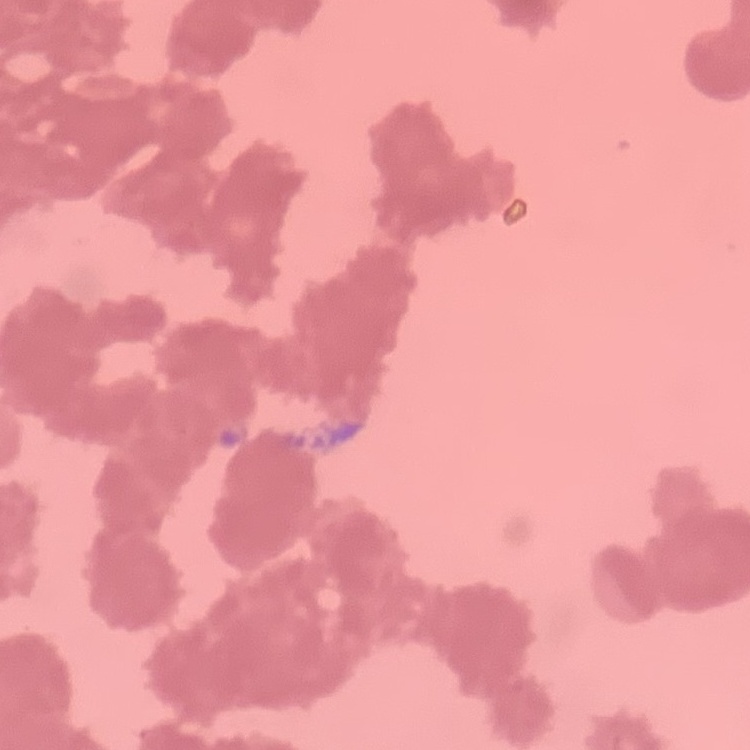

The erythrocytes show rouleaux formation. One tile cut from a larger photomicrograph. Stained with either Field's or Giemsa. Thin blood smear.